Assess the morphology of the red blood cells.
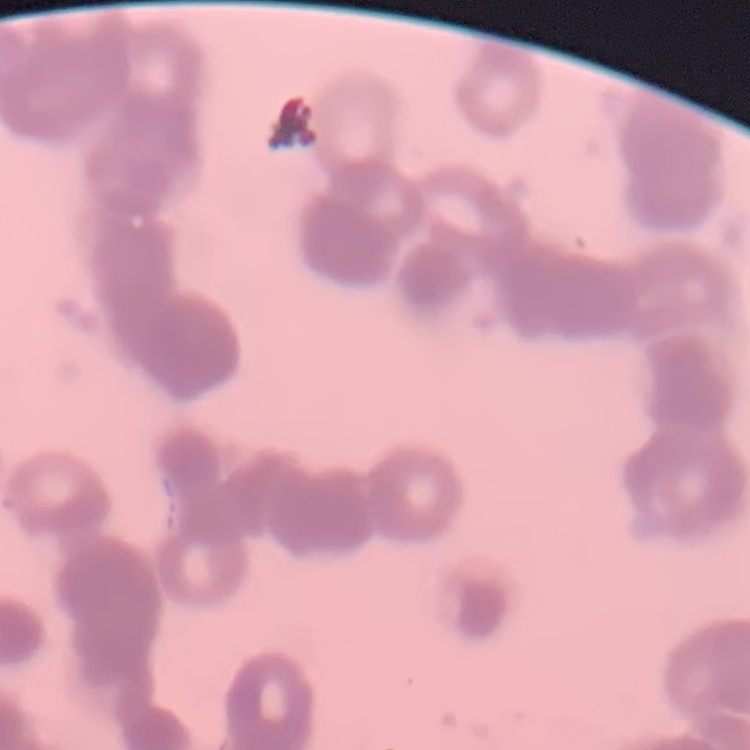
They show rouleaux formation.

Stained with either Field's or Giemsa. Thin blood film. One tile cut from a larger photomicrograph.